Locate every Trypanosoma brucei.
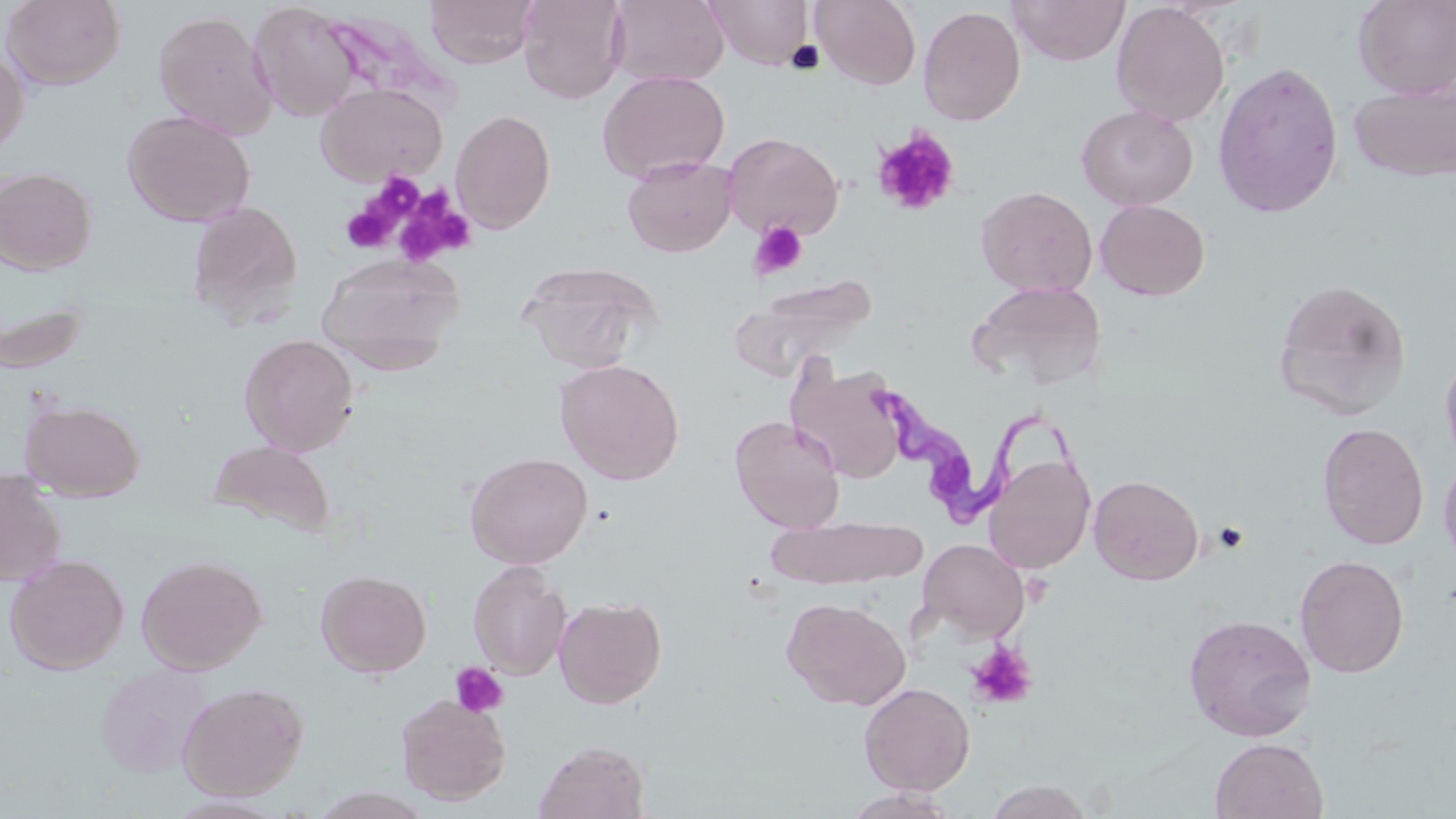
Approximate bounding boxes as named x1/y1/x2/y2 corners in pixels.
Trypanosoma brucei: (x1=866, y1=385, x2=1086, y2=530).

slide-level diagnosis = Trypanosoma brucei
magnification = 1000x
preparation = thin blood smear
platelet locations = approximate bounding boxes as named x1/y1/x2/y2 corners in pixels: (x1=871, y1=127, x2=960, y2=218), (x1=370, y1=170, x2=425, y2=215), (x1=391, y1=191, x2=474, y2=269), (x1=340, y1=199, x2=400, y2=254), (x1=750, y1=220, x2=808, y2=279), (x1=1211, y1=521, x2=1250, y2=554), (x1=966, y1=641, x2=1037, y2=710), (x1=450, y1=661, x2=507, y2=717)
stain = May-Grünwald-Giemsa
image size = 1456×819 pixels
field of view = single
uninfected red blood cell locations = approximate bounding boxes as named x1/y1/x2/y2 corners in pixels: (x1=2, y1=0, x2=125, y2=89), (x1=426, y1=0, x2=538, y2=68), (x1=517, y1=0, x2=627, y2=104), (x1=608, y1=0, x2=730, y2=88), (x1=705, y1=0, x2=814, y2=69), (x1=811, y1=0, x2=921, y2=90), (x1=1007, y1=0, x2=1131, y2=65), (x1=1353, y1=0, x2=1456, y2=98), (x1=248, y1=2, x2=361, y2=121), (x1=1111, y1=2, x2=1230, y2=125), (x1=918, y1=6, x2=1026, y2=126), (x1=153, y1=9, x2=278, y2=138), (x1=322, y1=12, x2=456, y2=114), (x1=0, y1=51, x2=28, y2=157), (x1=1212, y1=61, x2=1344, y2=219), (x1=598, y1=70, x2=730, y2=182), (x1=1348, y1=80, x2=1456, y2=183), (x1=316, y1=83, x2=446, y2=185), (x1=1077, y1=104, x2=1198, y2=210), (x1=122, y1=109, x2=256, y2=227), (x1=450, y1=110, x2=556, y2=233), (x1=722, y1=131, x2=843, y2=239), (x1=622, y1=155, x2=737, y2=256), (x1=0, y1=167, x2=97, y2=274), (x1=976, y1=185, x2=1097, y2=297), (x1=1095, y1=199, x2=1210, y2=300), (x1=187, y1=200, x2=303, y2=326), (x1=316, y1=252, x2=465, y2=372), (x1=517, y1=260, x2=659, y2=372), (x1=733, y1=275, x2=877, y2=377), (x1=1271, y1=279, x2=1412, y2=419), (x1=969, y1=280, x2=1107, y2=389), (x1=1, y1=293, x2=92, y2=374), (x1=239, y1=334, x2=359, y2=455), (x1=1439, y1=352, x2=1456, y2=471), (x1=556, y1=359, x2=685, y2=485), (x1=789, y1=364, x2=908, y2=483), (x1=21, y1=399, x2=144, y2=502), (x1=730, y1=415, x2=845, y2=533), (x1=1317, y1=422, x2=1429, y2=549), (x1=208, y1=439, x2=335, y2=538), (x1=464, y1=451, x2=593, y2=569), (x1=984, y1=454, x2=1095, y2=573), (x1=1438, y1=454, x2=1456, y2=570), (x1=0, y1=467, x2=68, y2=586), (x1=1089, y1=474, x2=1204, y2=585), (x1=768, y1=515, x2=926, y2=590), (x1=918, y1=539, x2=1029, y2=642), (x1=5, y1=553, x2=129, y2=674), (x1=1295, y1=553, x2=1409, y2=678), (x1=136, y1=555, x2=267, y2=674), (x1=468, y1=560, x2=571, y2=680), (x1=316, y1=569, x2=431, y2=678), (x1=554, y1=596, x2=667, y2=709), (x1=782, y1=597, x2=910, y2=710), (x1=1183, y1=614, x2=1317, y2=742), (x1=95, y1=664, x2=212, y2=778), (x1=177, y1=681, x2=308, y2=800), (x1=859, y1=682, x2=975, y2=794), (x1=395, y1=694, x2=511, y2=805), (x1=1210, y1=737, x2=1327, y2=819), (x1=534, y1=740, x2=650, y2=819), (x1=983, y1=779, x2=1096, y2=819), (x1=842, y1=788, x2=964, y2=818)
modality = light microscopy